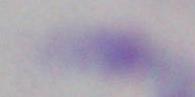

Micrograph. Toxoplasma gondii is shown. 1000x magnification.